Name the parasite shown.
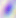

This is Toxoplasma gondii.

{
  "modality": "micrograph",
  "magnification": "400x"
}